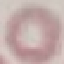 Result: no malaria parasites detected. Thin blood film. Giemsa-stained preparation. Acquired by smartphone through the microscope eyepiece. Cell patch, automatically extracted from a larger field of view and resized to 64 × 64 pixels.